Identify the parasite.
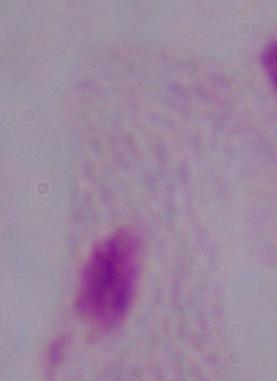
A trichomonad.

Summary:
  - Modality: micrograph
  - Magnification: 1000x